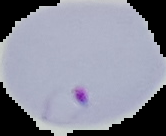
preparation = thin blood smear
image type = segmented cell region with the area outside set to black
result = Plasmodium parasites identified
image size = 166×136 pixels